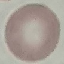
Summary:
  - Result: no malaria parasites detected
  - Image type: automatically extracted cell patch, resized to 64 × 64 pixels
  - Preparation: thin blood smear
  - Stain: Giemsa
  - Capture: smartphone through the microscope eyepiece